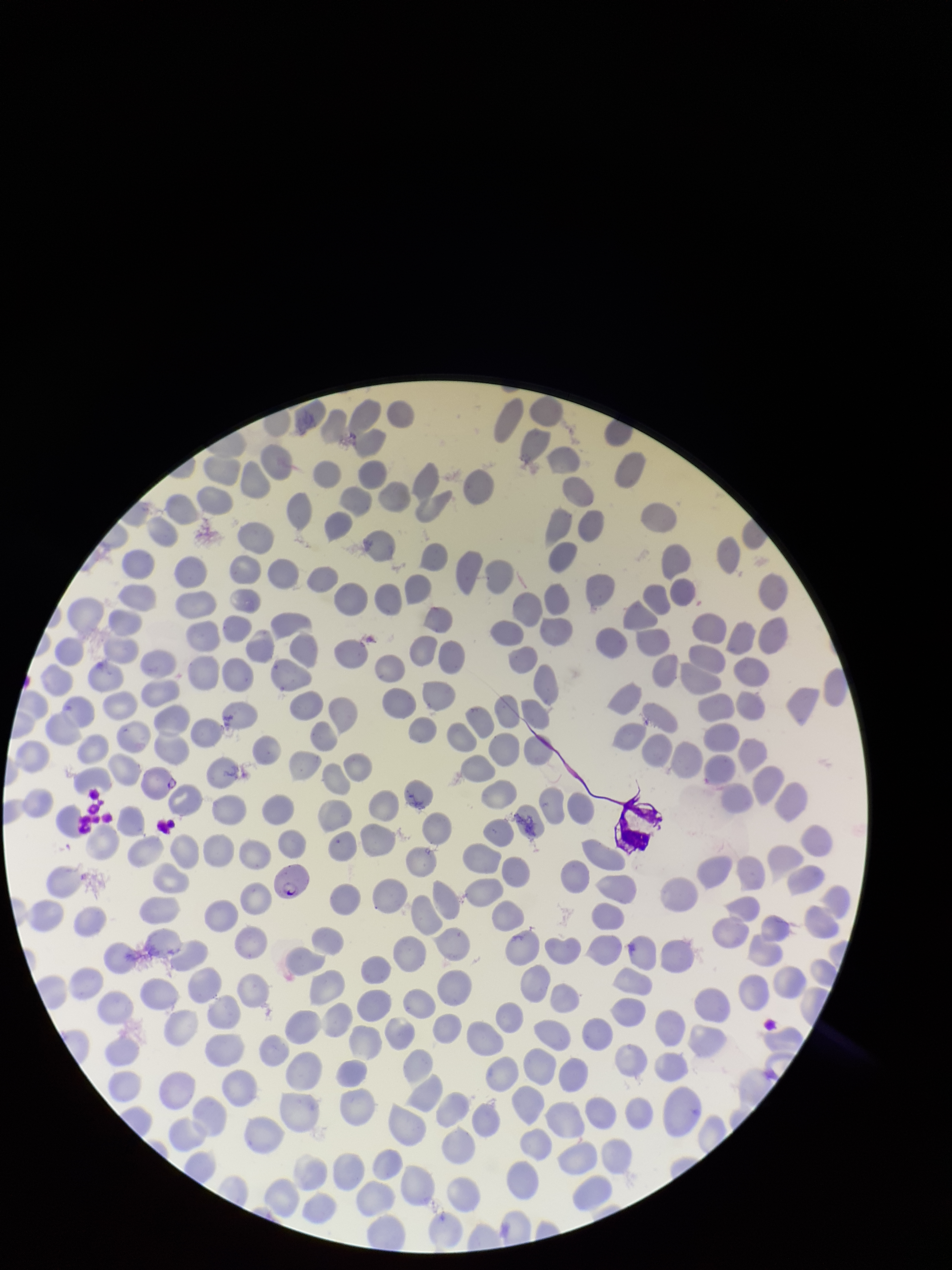
Summary:
  - Patient malaria status: infected
  - Parasitized red blood cell count: 1
  - Preparation: thin
  - Field of view: one from this slide
  - Red blood cell count: 240
  - Image size: 952×1270 pixels
  - Stain: Giemsa
  - Capture: smartphone photograph through the microscope eyepiece
  - Parasitized red blood cells: detected
  - Species reported for this patient: Plasmodium falciparum